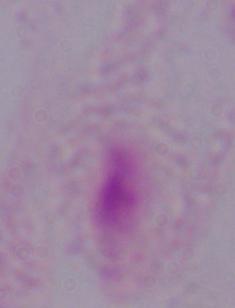

modality = micrograph
identification = trichomonad
magnification = 1000x